Assess for malaria.
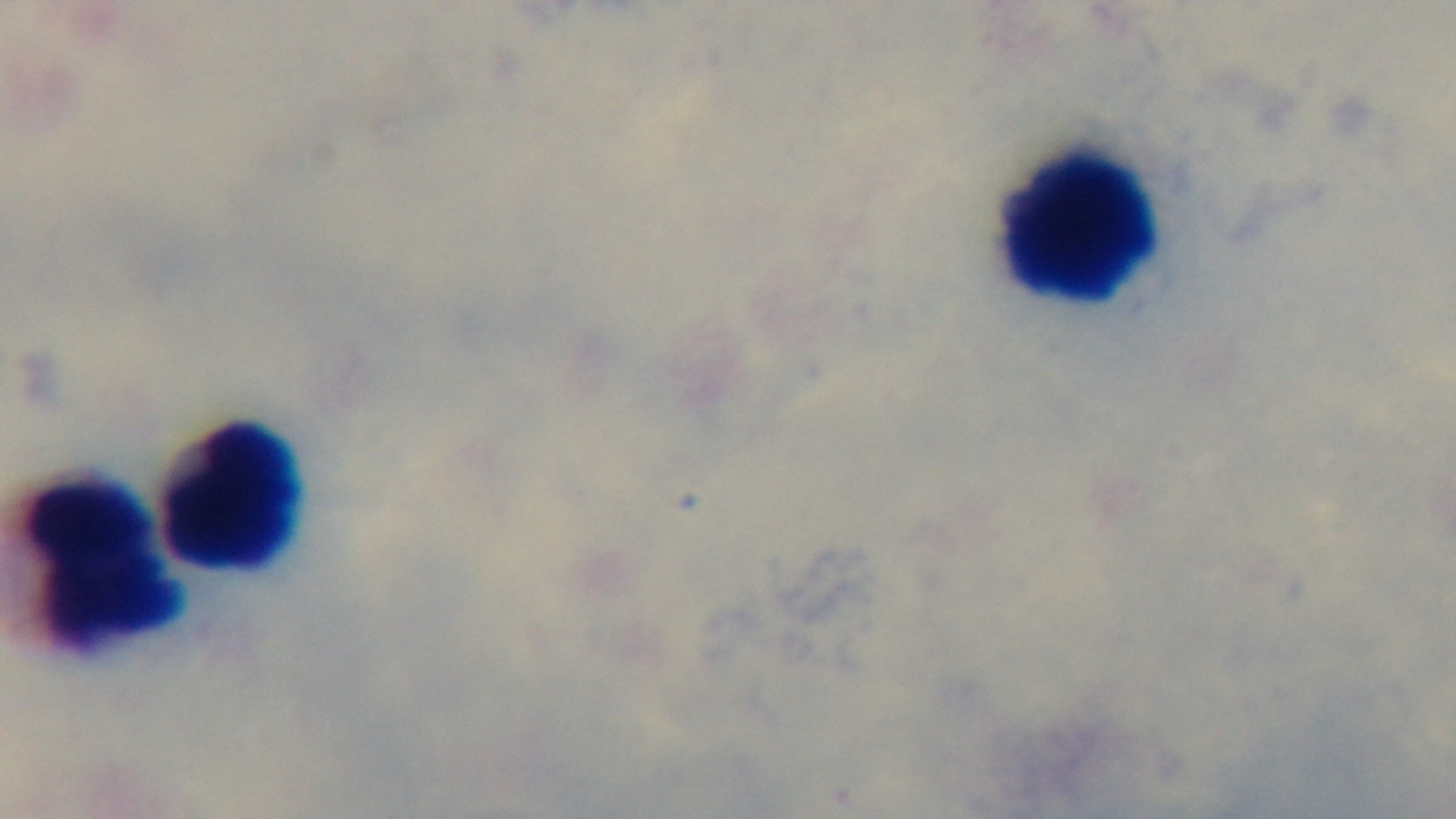
It is uninfected.

modality = light microscopy
capture = mounted 4K digital camera
field of view = single
objective = 100x oil immersion
stain = Giemsa
preparation = thick